Outline each blood parasite and name the species.
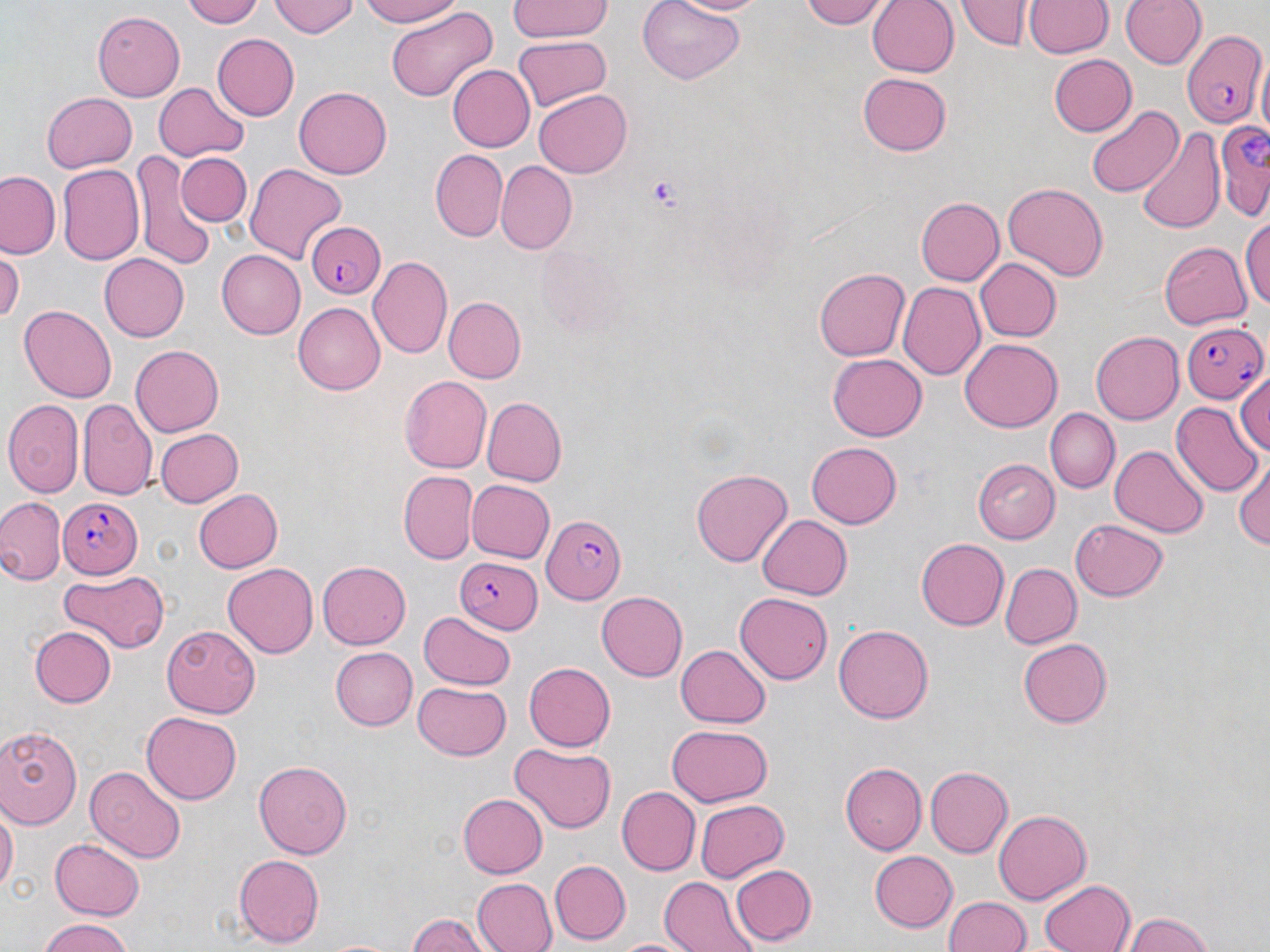

Approximate bounding boxes as (x1, y1, x2, y2) in pixels.
Plasmodium falciparum-infected red blood cells: (1181, 29, 1263, 129), (1217, 118, 1270, 220), (303, 222, 384, 299), (1181, 321, 1267, 401), (60, 494, 141, 580), (540, 515, 623, 600), (452, 557, 543, 634).
No Plasmodium ovale, Plasmodium malariae, Plasmodium vivax, Babesia divergens, or Trypanosoma brucei observed.

Summary:
  - Platelet locations: (649, 176, 682, 211)
  - Uninfected red blood cell locations: (185, 0, 264, 28), (272, 0, 359, 38), (354, 0, 466, 27), (507, 0, 614, 42), (638, 0, 746, 85), (668, 0, 771, 17), (799, 0, 892, 28), (867, 0, 959, 77), (956, 0, 1034, 51), (1026, 0, 1113, 57), (1122, 0, 1207, 72), (384, 6, 499, 105), (94, 11, 185, 100), (214, 34, 298, 118), (512, 35, 611, 112), (1048, 54, 1137, 137), (446, 66, 535, 152), (858, 73, 953, 156), (153, 83, 246, 164), (295, 88, 392, 179), (534, 88, 633, 176), (41, 92, 136, 172), (1088, 102, 1180, 197), (1135, 125, 1226, 236), (429, 149, 507, 241), (129, 151, 214, 267), (175, 151, 252, 228), (496, 160, 576, 252), (244, 164, 346, 266), (56, 165, 145, 266), (1, 170, 63, 260), (1003, 183, 1107, 282), (916, 196, 1004, 285), (1241, 214, 1270, 315), (1159, 238, 1252, 333), (0, 247, 24, 327), (215, 249, 306, 339), (100, 254, 190, 341), (369, 256, 452, 359), (975, 258, 1061, 341), (814, 267, 909, 362), (900, 282, 985, 380), (442, 296, 525, 384), (294, 302, 384, 395), (18, 305, 118, 402), (1089, 331, 1183, 426), (960, 339, 1062, 432), (130, 344, 224, 437), (829, 355, 927, 440), (1233, 374, 1270, 458), (400, 375, 492, 472), (482, 397, 567, 485), (3, 399, 85, 498), (78, 399, 156, 499), (1171, 403, 1261, 497), (1046, 410, 1119, 492), (154, 428, 243, 506), (806, 442, 902, 528), (1109, 445, 1208, 537), (1232, 452, 1270, 556), (975, 458, 1061, 544), (691, 468, 791, 568), (398, 472, 477, 563), (466, 480, 555, 563), (190, 486, 281, 574), (0, 498, 65, 585), (756, 513, 851, 598), (1069, 518, 1168, 600), (914, 538, 1008, 631), (224, 562, 320, 657), (318, 562, 410, 649), (1001, 562, 1081, 649), (62, 572, 166, 652), (597, 590, 688, 681), (735, 592, 834, 684), (417, 613, 515, 692), (833, 624, 934, 724), (163, 625, 260, 715), (28, 626, 115, 708), (1015, 637, 1116, 727), (677, 643, 771, 726), (331, 646, 416, 730), (524, 661, 618, 751), (413, 680, 511, 759), (141, 712, 241, 805), (0, 724, 83, 831), (666, 724, 773, 806), (508, 743, 616, 834), (254, 760, 354, 859), (840, 762, 925, 856), (86, 765, 187, 862), (925, 766, 1013, 856), (616, 786, 700, 875), (456, 793, 547, 877), (694, 800, 789, 882), (0, 801, 17, 901), (993, 809, 1090, 903), (51, 836, 145, 918), (869, 851, 956, 932), (233, 853, 324, 947), (550, 860, 631, 943), (729, 863, 815, 947), (470, 877, 558, 952), (659, 877, 751, 952), (1039, 878, 1134, 952), (945, 895, 1031, 952), (1125, 912, 1218, 952), (406, 913, 489, 952), (37, 920, 137, 952), (611, 937, 693, 952)
  - Slide-level diagnosis: Plasmodium falciparum
  - Image size: 1270×952 pixels
  - Field of view: one of a larger specimen
  - Stain: May-Grünwald-Giemsa
  - Magnification: 1000x
  - Modality: light microscopy
  - Preparation: thin blood smear